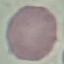 Result: no malaria parasites seen. Thin smear of blood. Photographed with a smartphone camera at the microscope eyepiece. Giemsa stain. Automatically extracted cell patch, resized to 64 × 64 pixels.